Name the parasite shown.
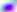

Toxoplasma gondii.

Summary:
  - Modality: photomicrograph
  - Magnification: 400x